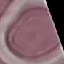

{
  "malaria_status": "uninfected",
  "image_type": "cell patch, automatically extracted from a larger field of view and resized to 64 × 64 pixels",
  "capture": "smartphone through the microscope eyepiece",
  "stain": "Giemsa",
  "preparation": "thin blood film"
}